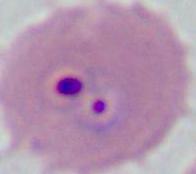
Summary:
  - Identification: Plasmodium
  - Modality: micrograph
  - Magnification: 400x or 1000x